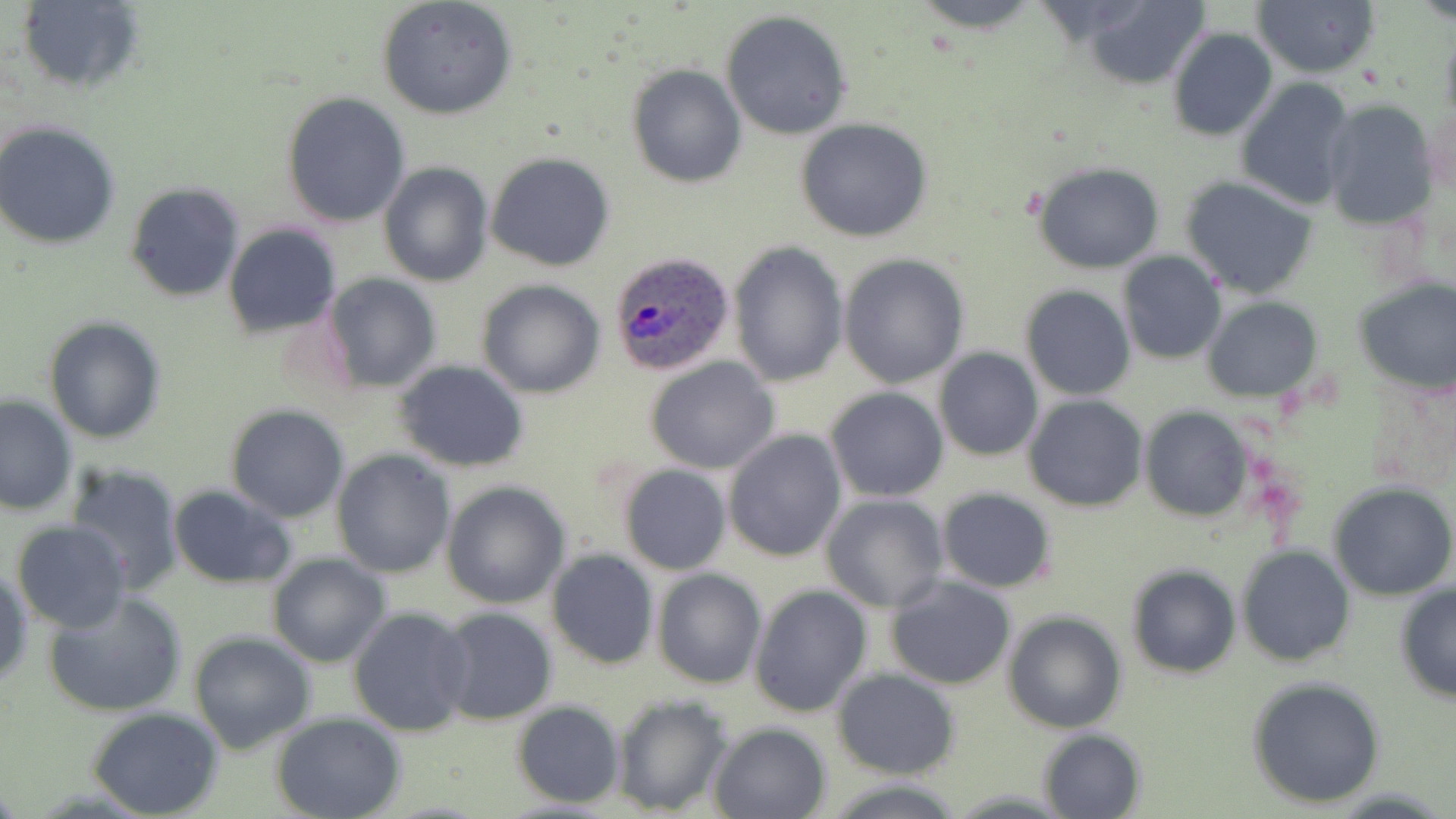

Summary:
  - Coordinate format: approximate bounding boxes as named x1/y1/x2/y2 corners in pixels
  - Plasmodium ovale-infected red blood cell locations: (x1=608, y1=253, x2=735, y2=378)
  - Uninfected red blood cell locations: (x1=15, y1=0, x2=145, y2=96), (x1=376, y1=0, x2=518, y2=120), (x1=907, y1=0, x2=1048, y2=31), (x1=1251, y1=0, x2=1379, y2=79), (x1=1072, y1=1, x2=1212, y2=86), (x1=720, y1=10, x2=853, y2=140), (x1=1439, y1=24, x2=1456, y2=131), (x1=1167, y1=26, x2=1277, y2=141), (x1=626, y1=64, x2=747, y2=187), (x1=1236, y1=77, x2=1358, y2=211), (x1=282, y1=91, x2=412, y2=228), (x1=1321, y1=100, x2=1438, y2=231), (x1=795, y1=118, x2=933, y2=243), (x1=0, y1=124, x2=120, y2=249), (x1=485, y1=152, x2=616, y2=272), (x1=378, y1=161, x2=493, y2=286), (x1=1033, y1=163, x2=1165, y2=274), (x1=1181, y1=176, x2=1321, y2=298), (x1=125, y1=181, x2=246, y2=301), (x1=223, y1=224, x2=341, y2=336), (x1=728, y1=243, x2=848, y2=387), (x1=1118, y1=251, x2=1226, y2=365), (x1=840, y1=255, x2=969, y2=389), (x1=321, y1=274, x2=443, y2=392), (x1=1352, y1=278, x2=1456, y2=394), (x1=477, y1=279, x2=605, y2=399), (x1=1020, y1=284, x2=1135, y2=401), (x1=1202, y1=297, x2=1322, y2=402), (x1=44, y1=316, x2=165, y2=444), (x1=934, y1=347, x2=1043, y2=461), (x1=645, y1=356, x2=781, y2=474), (x1=393, y1=361, x2=530, y2=473), (x1=825, y1=386, x2=949, y2=501), (x1=1, y1=395, x2=78, y2=515), (x1=1023, y1=395, x2=1148, y2=513), (x1=224, y1=404, x2=349, y2=523), (x1=1139, y1=406, x2=1251, y2=524), (x1=724, y1=429, x2=848, y2=562), (x1=331, y1=450, x2=454, y2=577), (x1=62, y1=462, x2=185, y2=594), (x1=617, y1=463, x2=731, y2=574), (x1=440, y1=481, x2=570, y2=608), (x1=1329, y1=483, x2=1456, y2=601), (x1=168, y1=485, x2=297, y2=587), (x1=936, y1=488, x2=1058, y2=593), (x1=820, y1=493, x2=949, y2=612), (x1=12, y1=520, x2=131, y2=632), (x1=1236, y1=544, x2=1354, y2=668), (x1=546, y1=549, x2=658, y2=670), (x1=266, y1=554, x2=389, y2=668), (x1=1125, y1=564, x2=1242, y2=679), (x1=1, y1=566, x2=32, y2=690), (x1=652, y1=568, x2=766, y2=688), (x1=885, y1=574, x2=1017, y2=689), (x1=1394, y1=582, x2=1456, y2=705), (x1=749, y1=584, x2=872, y2=718), (x1=44, y1=591, x2=188, y2=718), (x1=348, y1=606, x2=475, y2=739), (x1=436, y1=606, x2=558, y2=725), (x1=1002, y1=610, x2=1127, y2=734), (x1=187, y1=632, x2=315, y2=755), (x1=833, y1=669, x2=958, y2=777), (x1=1245, y1=676, x2=1388, y2=809), (x1=611, y1=693, x2=734, y2=817), (x1=511, y1=701, x2=625, y2=806), (x1=87, y1=708, x2=224, y2=819), (x1=272, y1=713, x2=405, y2=819), (x1=708, y1=722, x2=832, y2=818), (x1=1036, y1=726, x2=1147, y2=818), (x1=821, y1=778, x2=970, y2=817)
  - Slide-level diagnosis: Plasmodium ovale
  - Stain: May-Grünwald-Giemsa
  - Image size: 1456×819 pixels
  - Modality: light microscopy
  - Field of view: single
  - Preparation: thin blood film
  - Magnification: 1000x